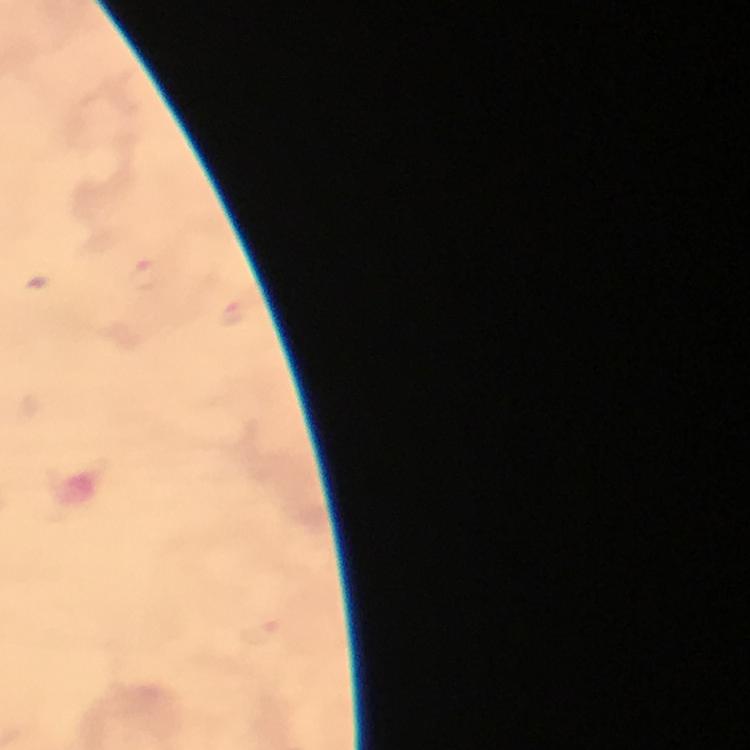

{
  "image_size": "750×750 pixels",
  "stain": "Giemsa",
  "capture": "smartphone photograph through a microscope",
  "immersion_oil": "used",
  "plasmodium_parasite_locations": "approximate centers as [x, y] in pixels: [145, 276], [235, 313], [260, 631]",
  "context": "from a diagnostic examination for malaria",
  "cropped_from": "one field of view",
  "preparation": "thick blood smear",
  "magnification": "100x"
}